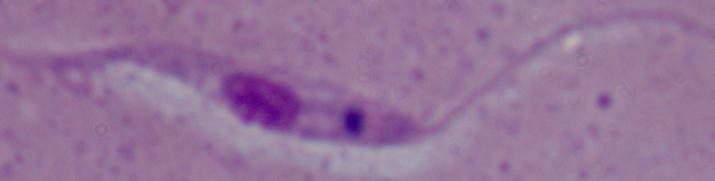

Captured at 1000x magnification. A Leishmania parasite is seen. Micrograph.